Assess this cell for malaria.
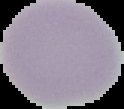
It is uninfected.

Summary:
  - Preparation: thin blood film
  - Image type: cell region segmented out of the field of view; surrounding area masked to black
  - Image size: 124×109 pixels